Name the blood parasite species.
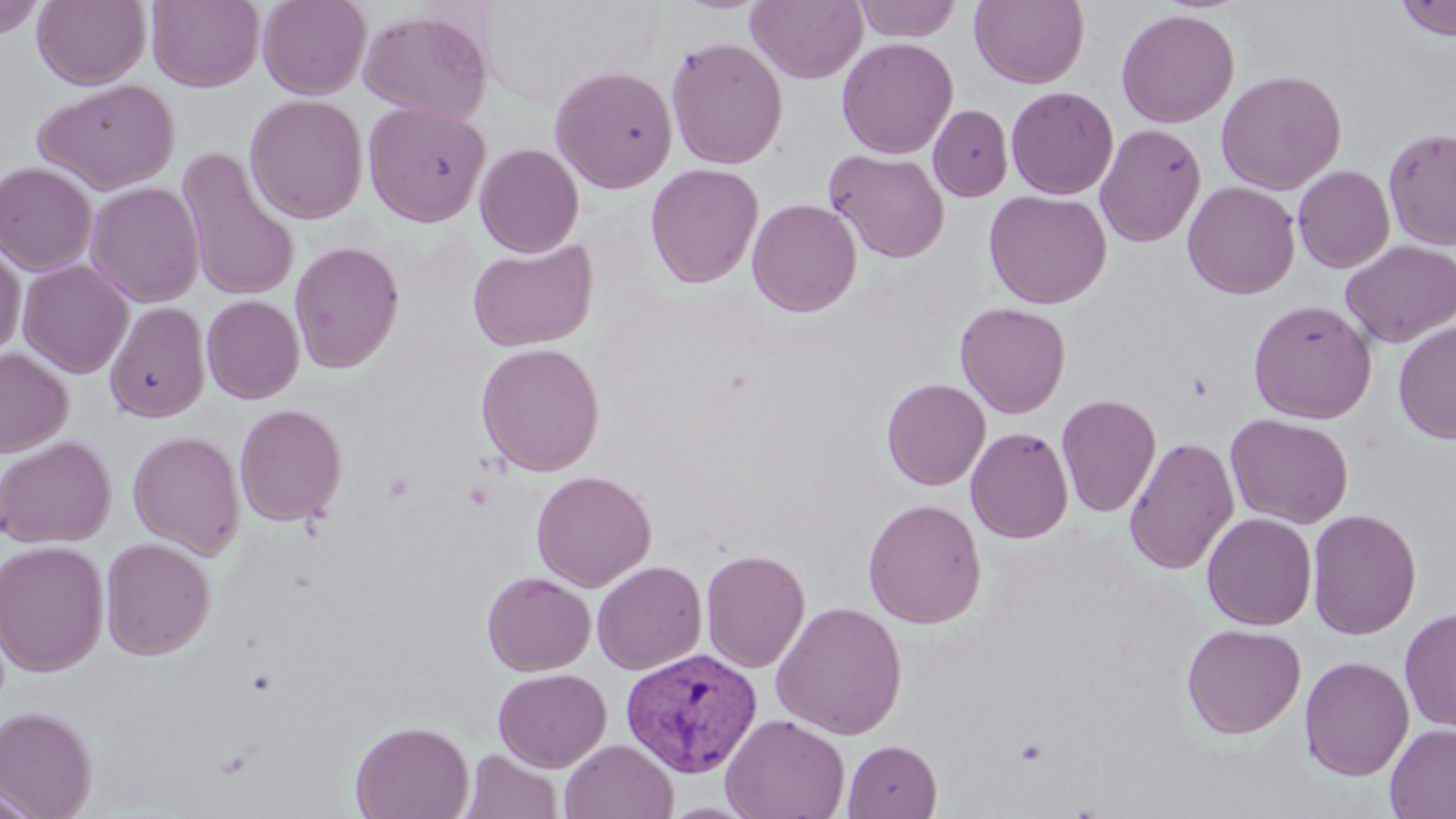

Plasmodium vivax.

Approximate bounding boxes as [x1, y1, x2, y2] in pixels. Plasmodium vivax-infected red blood cell locations: [620, 647, 763, 778]. Uninfected red blood cell locations: [0, 0, 47, 39], [32, 0, 151, 90], [146, 0, 265, 92], [257, 0, 371, 100], [853, 0, 963, 42], [970, 0, 1088, 89], [1394, 0, 1456, 41], [746, 1, 867, 84], [1115, 7, 1239, 128], [358, 8, 494, 123], [665, 35, 788, 170], [836, 37, 958, 159], [549, 64, 678, 193], [1216, 69, 1346, 195], [33, 79, 180, 194], [1005, 86, 1119, 199], [245, 94, 367, 224], [362, 101, 491, 227], [928, 104, 1013, 202], [1095, 123, 1206, 247], [1383, 127, 1456, 251], [474, 143, 584, 257], [176, 148, 301, 303], [824, 148, 950, 264], [0, 162, 98, 276], [645, 163, 763, 288], [1293, 165, 1396, 273], [85, 181, 205, 307], [1182, 181, 1301, 299], [984, 189, 1112, 309], [747, 198, 862, 317], [1, 235, 26, 356], [467, 237, 598, 352], [1341, 240, 1455, 347], [288, 241, 405, 373], [17, 259, 134, 378], [201, 294, 305, 404], [1248, 298, 1377, 424], [104, 301, 210, 423], [955, 302, 1071, 418], [1394, 320, 1456, 445], [475, 342, 605, 476], [0, 347, 73, 457], [881, 377, 991, 491], [1056, 392, 1161, 518], [234, 402, 347, 526], [1225, 413, 1354, 529], [965, 426, 1074, 543], [128, 430, 246, 560], [0, 436, 116, 548], [1123, 436, 1239, 575], [531, 469, 657, 591], [862, 497, 987, 629], [1307, 507, 1422, 639], [1202, 512, 1317, 630], [101, 537, 215, 660], [0, 539, 109, 676], [700, 548, 811, 673], [592, 560, 708, 675], [482, 571, 596, 676], [771, 600, 907, 739], [1400, 606, 1456, 734], [1181, 623, 1306, 739], [1300, 655, 1414, 781], [493, 668, 612, 772], [0, 705, 97, 818], [720, 713, 850, 819], [350, 719, 474, 819], [1385, 723, 1456, 818], [560, 738, 678, 819], [843, 739, 942, 819], [460, 748, 563, 819], [0, 777, 46, 818]. Platelet locations: [1013, 736, 1050, 765]. Optical microscopy. May-Grünwald-Giemsa stain. Thin blood smear. Single field of view. 1000x magnification. Image is 1456×819 pixels.